Report the malaria status of this cell.
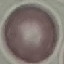

Uninfected.

image_type: cell patch, automatically extracted from a larger field of view and resized to 64 × 64 pixels
capture: smartphone camera at the microscope eyepiece
preparation: thin smear
stain: Giemsa